Identify the parasite.
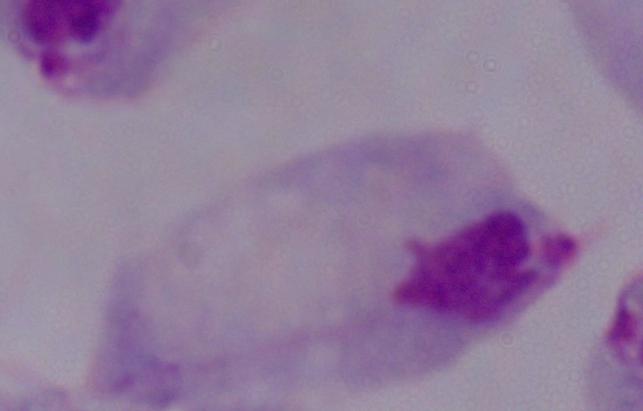
A trichomonad.

{
  "modality": "micrograph",
  "magnification": "1000x"
}